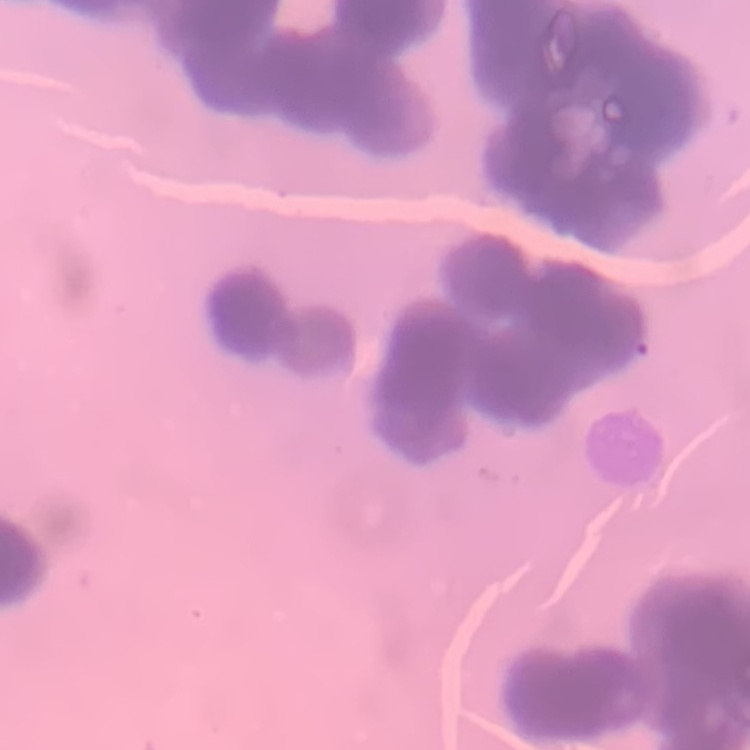 The erythrocytes exhibit rouleaux formation. Square crop of a larger photomicrograph. Stained with either Field's or Giemsa. Thin blood smear.